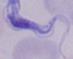
Captured at 1000x magnification. A trypanosome is shown. Photomicrograph.